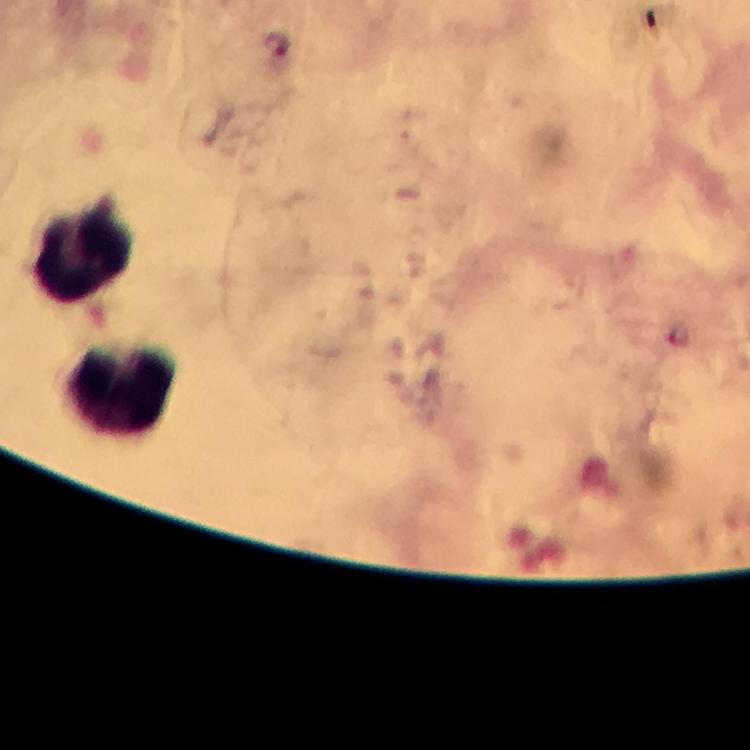

stain: Giemsa
context: from a diagnostic examination for malaria
plasmodium_parasite_locations: 'approximate object centers, in pixels from the top-left corner: (x=276, y=45)'
capture: smartphone photograph through a microscope
image_size: 750×750 pixels
magnification: 100x
leukocyte_locations: 'approximate object centers, in pixels from the top-left corner: (x=82, y=249), (x=121, y=391)'
immersion_oil: applied
preparation: thick blood smear
cropped_from: one field of view